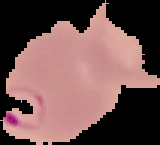

Summary:
  - Preparation: thin blood smear
  - Image type: segmented cell region with the area outside set to black
  - Image size: 160×145 pixels
  - Malaria status: parasitized